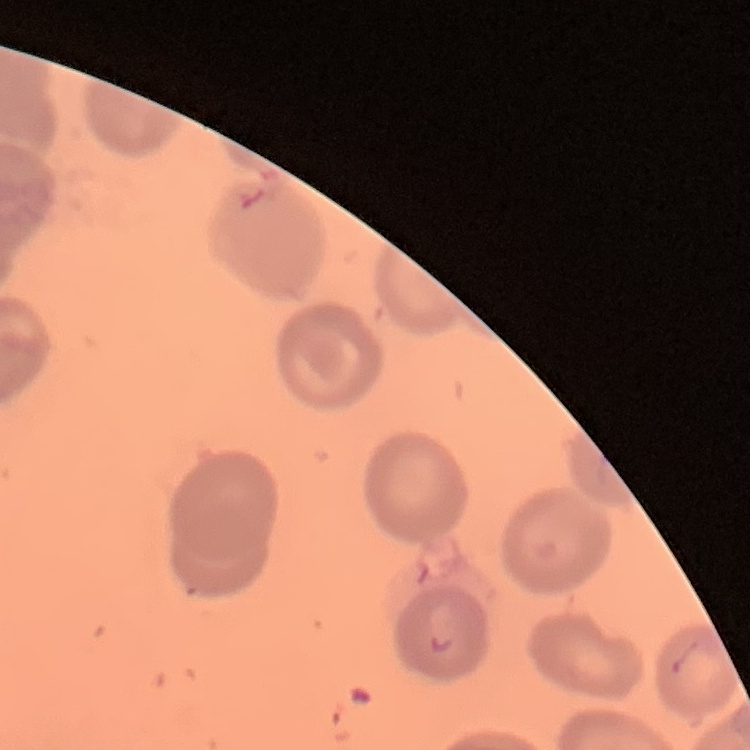
The erythrocytes exhibit no rouleaux formation. One tile cut from a larger photomicrograph. Stained with either Field's or Giemsa. Thin blood smear.